Identify the parasite.
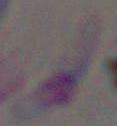
Toxoplasma gondii.

Summary:
  - Modality: micrograph
  - Magnification: 1000x